State which cell type is depicted.
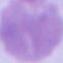
An erythrocyte.

modality = photomicrograph
magnification = 1000x